Give the extent of all Plasmodium falciparum-infected red blood cells.
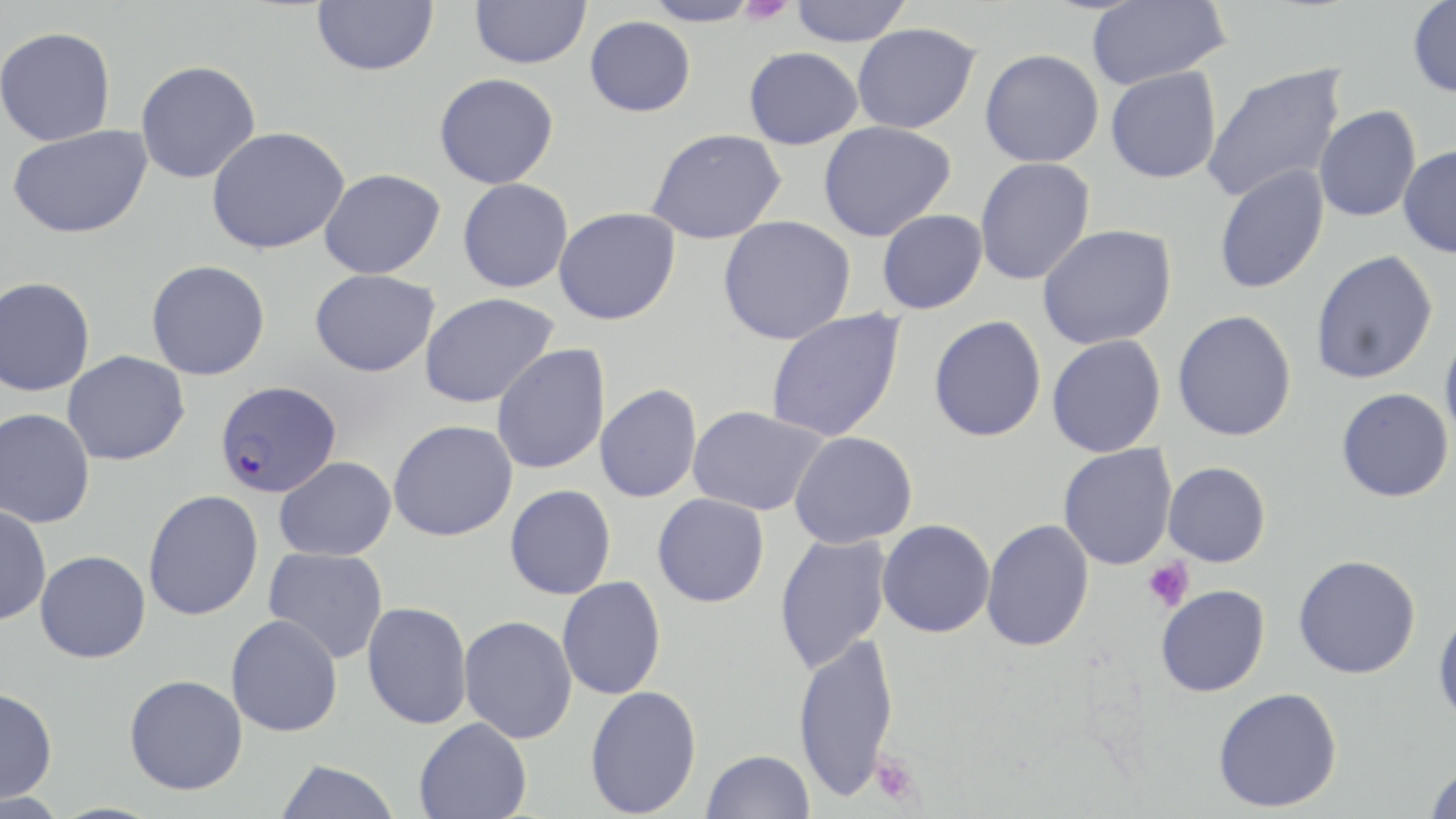

Approximate bounding boxes as [x1, y1, x2, y2] in pixels.
Plasmodium falciparum-infected red blood cells: [215, 380, 342, 498].

{
  "slide_level_diagnosis": "Plasmodium falciparum",
  "image_size": "1456×819 pixels",
  "platelet_locations": "approximate bounding boxes as [x1, y1, x2, y2] in pixels: [738, 0, 794, 26], [1142, 558, 1194, 612], [869, 752, 923, 808]",
  "uninfected_red_blood_cell_locations": "approximate bounding boxes as [x1, y1, x2, y2] in pixels: [311, 0, 439, 76], [469, 0, 591, 69], [640, 0, 764, 27], [788, 0, 913, 46], [1086, 0, 1230, 89], [1407, 0, 1456, 98], [585, 16, 696, 117], [851, 22, 980, 134], [0, 26, 116, 146], [743, 46, 863, 149], [980, 49, 1104, 167], [135, 60, 261, 184], [1202, 63, 1347, 204], [1105, 67, 1222, 184], [434, 73, 559, 189], [1314, 105, 1421, 222], [818, 121, 956, 241], [7, 124, 152, 239], [206, 126, 350, 255], [646, 128, 787, 244], [1398, 145, 1456, 259], [974, 157, 1095, 286], [1213, 164, 1329, 295], [319, 168, 446, 278], [457, 178, 573, 293], [553, 207, 680, 325], [877, 209, 988, 314], [718, 215, 857, 345], [1037, 225, 1177, 350], [1310, 249, 1438, 385], [146, 260, 270, 380], [310, 268, 440, 377], [0, 276, 95, 397], [420, 293, 559, 408], [765, 309, 906, 442], [1172, 310, 1297, 441], [929, 315, 1047, 442], [1439, 326, 1456, 448], [1046, 335, 1166, 457], [491, 344, 611, 475], [61, 350, 189, 466], [595, 383, 702, 503], [1336, 388, 1454, 502], [687, 405, 827, 516], [0, 408, 96, 529], [388, 420, 518, 542], [789, 431, 918, 549], [1058, 443, 1177, 570], [274, 457, 397, 561], [1163, 461, 1271, 567], [505, 484, 616, 599], [143, 489, 264, 621], [652, 493, 770, 607], [0, 504, 51, 626], [981, 518, 1094, 652], [877, 519, 996, 638], [774, 532, 891, 673], [263, 547, 389, 664], [35, 550, 151, 663], [1293, 555, 1421, 679], [557, 576, 666, 700], [1155, 584, 1270, 697], [362, 601, 472, 730], [1432, 609, 1456, 725], [225, 614, 343, 737], [459, 615, 578, 744], [792, 632, 899, 802], [124, 674, 248, 795], [584, 684, 702, 817], [0, 687, 58, 805], [1213, 687, 1342, 813], [414, 717, 532, 819], [701, 749, 816, 819], [273, 759, 400, 819], [1423, 764, 1456, 818]",
  "magnification": "1000x",
  "modality": "optical microscopy",
  "preparation": "thin blood film",
  "stain": "May-Grünwald-Giemsa",
  "field_of_view": "one of a larger specimen"
}